Locate and identify every blood parasite.
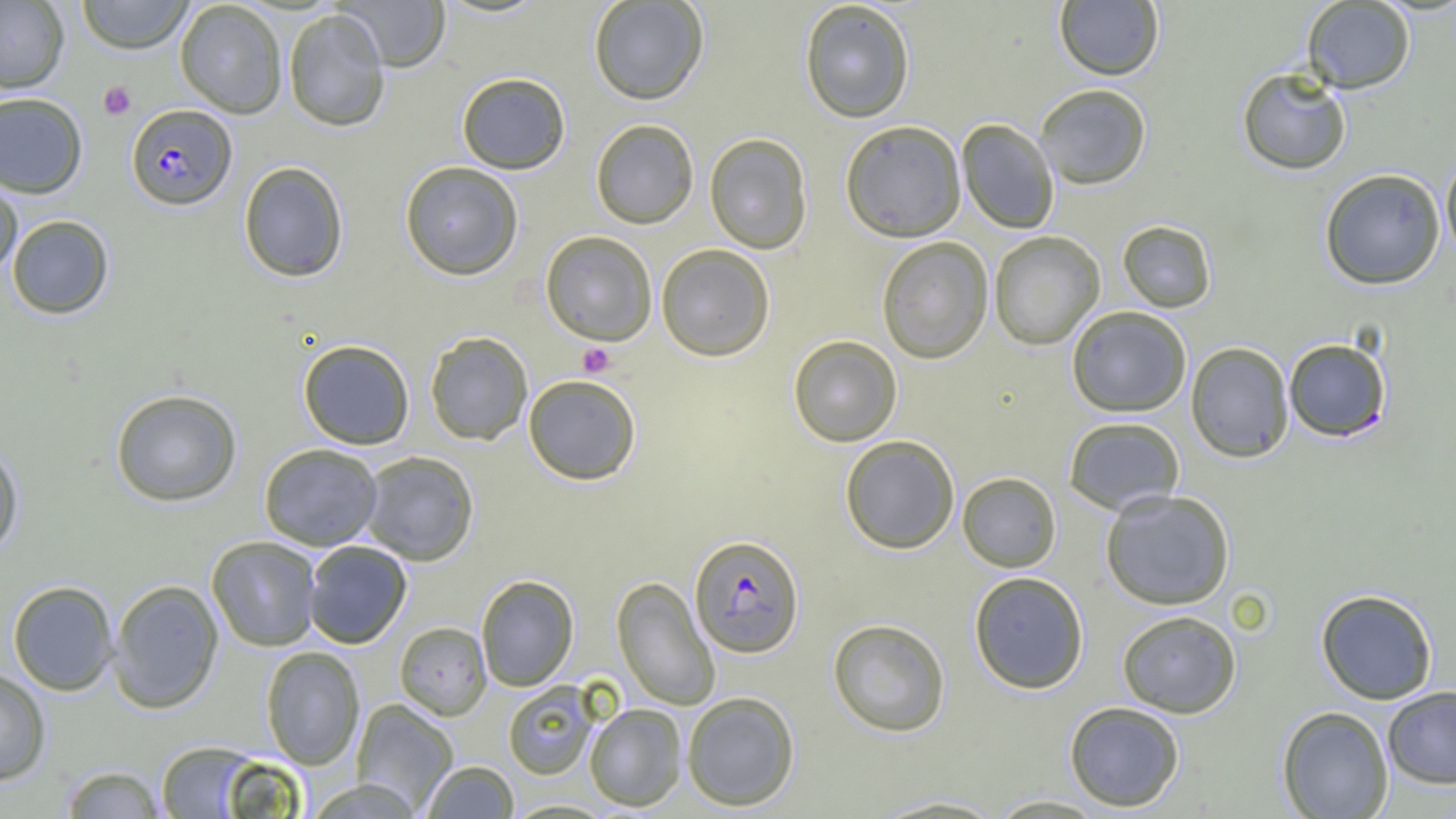
Approximate bounding boxes as (x1,y1)-(x2,y2) corner pairs in pixels.
Plasmodium falciparum-infected red blood cells: (126,104)-(237,210), (689,534)-(804,658).
No Plasmodium ovale, Plasmodium malariae, Plasmodium vivax, Babesia divergens, or Trypanosoma brucei observed.

{
  "slide_level_diagnosis": "Plasmodium falciparum",
  "platelet_locations": "approximate bounding boxes as (x1,y1)-(x2,y2) corner pairs in pixels: (98,81)-(136,120), (578,342)-(616,377)",
  "field_of_view": "one of a larger specimen",
  "uninfected_red_blood_cell_locations": "approximate bounding boxes as (x1,y1)-(x2,y2) corner pairs in pixels: (0,0)-(69,93), (76,0)-(194,53), (588,0)-(709,105), (175,1)-(288,119), (337,1)-(451,72), (799,1)-(916,123), (1054,1)-(1164,80), (1301,1)-(1415,93), (283,8)-(391,132), (1237,67)-(1352,175), (456,72)-(571,174), (1034,83)-(1152,189), (0,92)-(88,198), (590,119)-(699,229), (956,119)-(1060,233), (840,120)-(967,242), (704,133)-(812,253), (1440,152)-(1456,264), (238,161)-(349,283), (399,161)-(524,280), (1319,168)-(1446,290), (0,178)-(23,280), (7,215)-(114,319), (1117,220)-(1217,312), (540,230)-(658,345), (989,230)-(1105,350), (876,236)-(994,364), (655,243)-(775,361), (1066,306)-(1192,417), (424,331)-(533,445), (788,335)-(902,447), (1283,338)-(1392,442), (298,339)-(415,450), (1185,341)-(1295,462), (523,374)-(642,486), (110,388)-(242,506), (1062,416)-(1185,515), (840,434)-(960,554), (0,440)-(25,561), (259,443)-(383,551), (358,451)-(479,565), (957,471)-(1062,572), (1100,489)-(1235,610), (206,536)-(321,651), (303,540)-(412,648), (968,571)-(1089,693), (476,575)-(579,692), (612,576)-(720,711), (108,578)-(224,713), (8,580)-(119,695), (1315,589)-(1438,704), (1117,610)-(1241,718), (827,618)-(951,737), (394,621)-(491,721), (261,646)-(365,769), (0,667)-(52,785), (503,681)-(601,779), (1381,686)-(1456,789), (682,691)-(800,811), (351,698)-(458,813), (1064,701)-(1185,811), (585,703)-(687,811), (1277,706)-(1393,818), (154,740)-(273,818), (421,761)-(519,818), (60,765)-(166,818), (304,778)-(424,819), (864,794)-(1011,818), (984,794)-(1109,817)",
  "image_size": "1456×819 pixels",
  "magnification": "1000x",
  "preparation": "thin blood film",
  "modality": "optical microscopy"
}